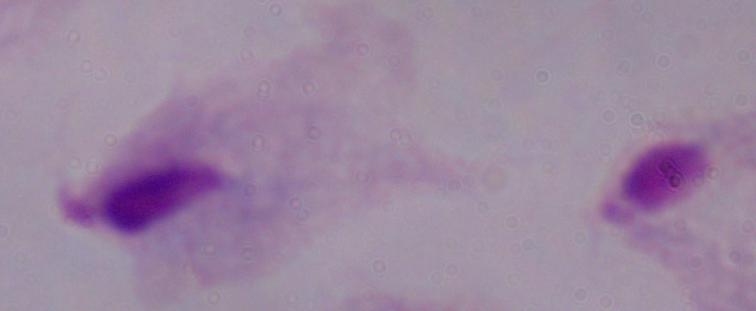

Summary:
  - Magnification: 1000x
  - Modality: photomicrograph
  - Identification: trichomonad